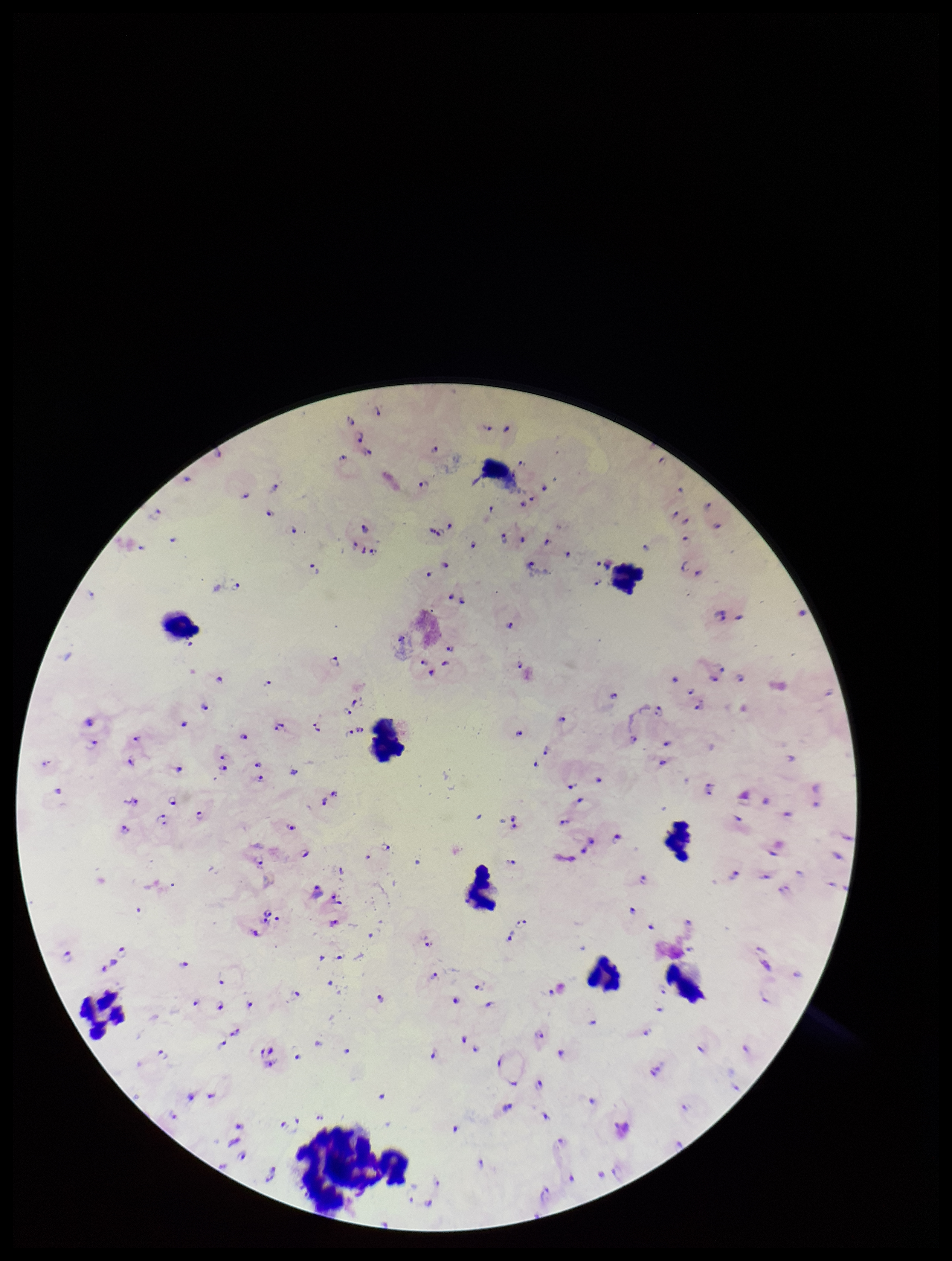

preparation = thick
capture = smartphone photograph through the microscope eyepiece
image size = 952×1261 pixels
parasite count = 90
stain = Giemsa
patient malaria status = positive
species reported for this patient = Plasmodium falciparum
leukocyte count = 10
field of view = one from this slide
Plasmodium parasites = detected